Name the parasite shown.
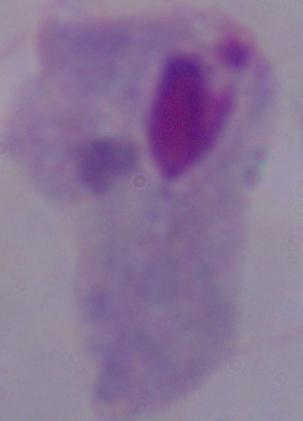
A trichomonad.

{
  "modality": "micrograph",
  "magnification": "1000x"
}